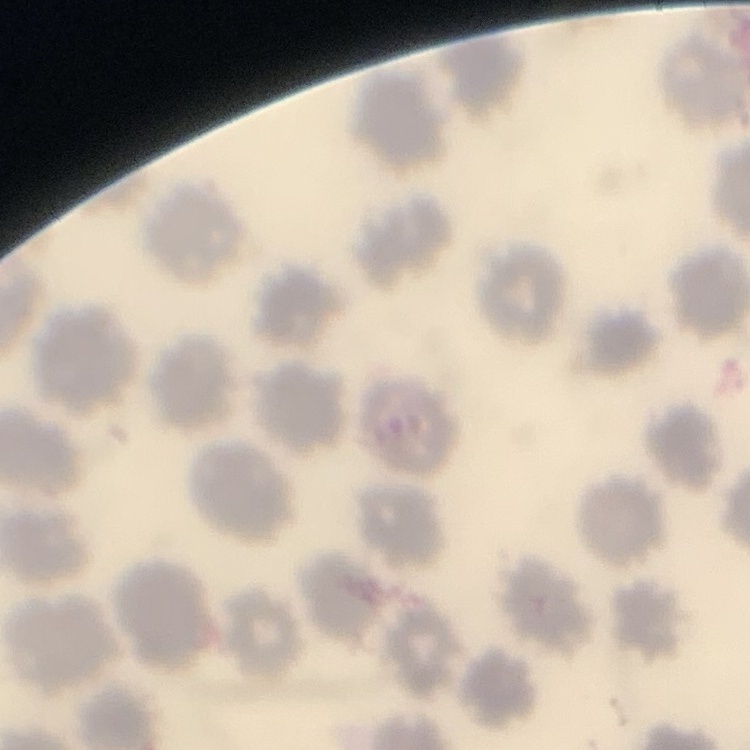

Summary:
  - Erythrocyte morphology: no rouleaux formation
  - Stain: Field's or Giemsa
  - Preparation: thin blood film
  - Image type: one tile cut from a larger photomicrograph